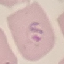
Malaria status: parasitized. Acquired by smartphone through the microscope eyepiece. Automatically extracted cell patch, resized to 64 × 64 pixels. Giemsa stain. Thin blood film.